Assess this cell for malaria.
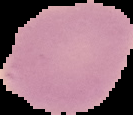
It is uninfected.

image size = 133×115 pixels
preparation = thin blood smear
image type = cell region segmented out of the field of view; surrounding area masked to black